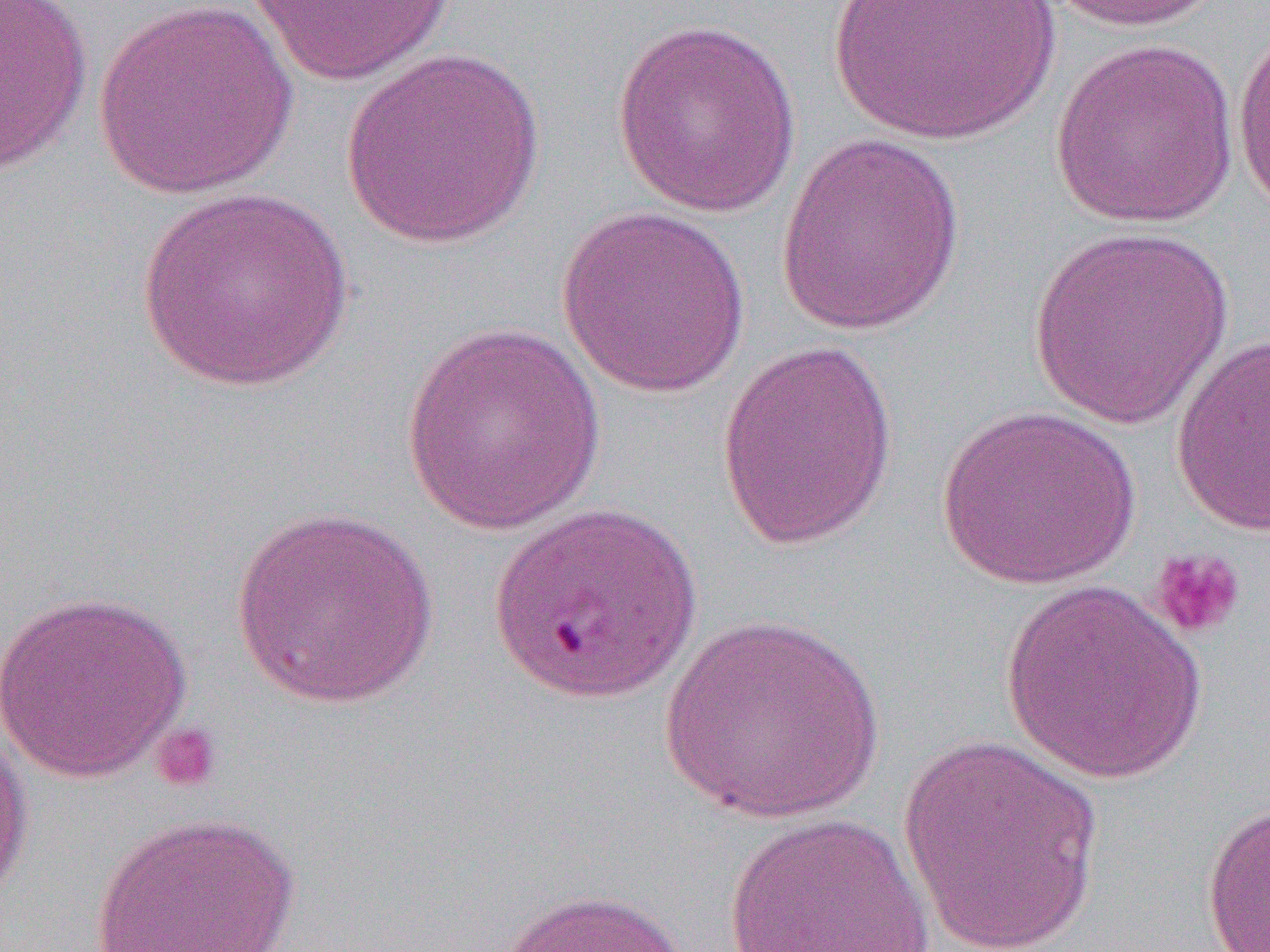

Summary:
  - Coordinate format: approximate bounding boxes as [x1, y1, x2, y2] in pixels
  - Platelet locations: [1146, 547, 1247, 642], [148, 722, 223, 793]
  - Uninfected red blood cell locations: [0, 0, 94, 176], [828, 0, 1058, 148], [1045, 0, 1227, 33], [243, 1, 457, 86], [92, 2, 301, 199], [1231, 15, 1270, 219], [610, 18, 802, 217], [1049, 38, 1242, 228], [339, 48, 546, 250], [775, 132, 966, 337], [134, 185, 356, 393], [557, 205, 751, 397], [1026, 227, 1237, 430], [398, 324, 606, 534], [1170, 334, 1270, 536], [716, 339, 899, 551], [935, 404, 1141, 589], [228, 507, 441, 708], [999, 581, 1209, 783], [0, 588, 194, 783], [659, 612, 886, 825], [0, 719, 34, 914], [899, 732, 1103, 951], [1201, 801, 1270, 951], [89, 811, 301, 952], [721, 813, 936, 952], [494, 888, 694, 952]
  - Slide-level diagnosis: Plasmodium falciparum
  - Preparation: thin blood film
  - Field of view: one of a larger specimen
  - Image size: 1270×952 pixels
  - Modality: optical microscopy
  - Magnification: 1000x